Point out each malaria parasite.
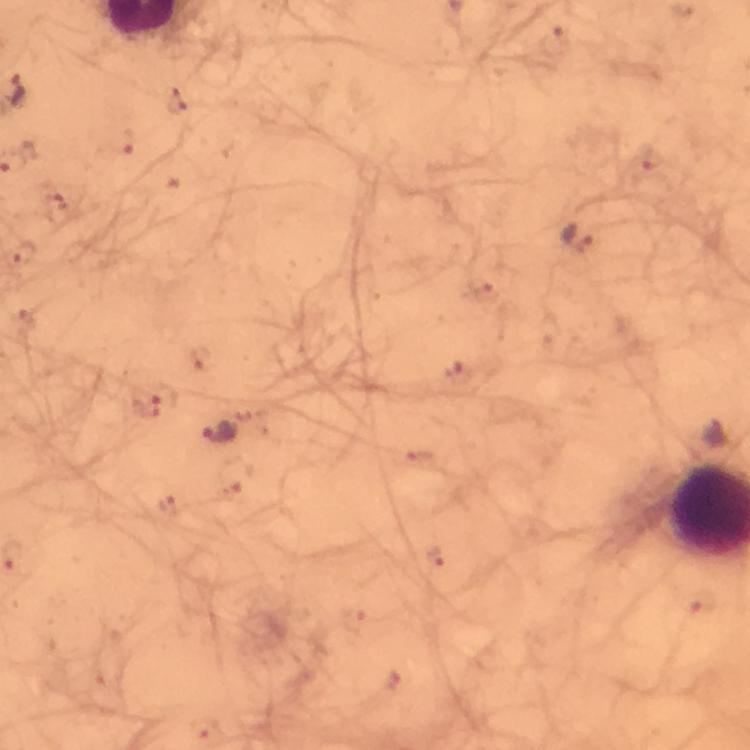

Approximate centers as {x, y} in pixels.
Malaria parasites: {555, 42}, {177, 103}, {126, 144}, {647, 159}, {54, 204}, {578, 238}, {24, 252}, {480, 286}, {201, 358}, {458, 373}, {147, 406}, {219, 432}, {423, 461}, {170, 505}, {435, 558}, {353, 622}, {204, 728}.

Giemsa-stained preparation. Photographed with a smartphone mounted on the microscope. Immersion oil applied. From a malaria diagnostic workup. Thick smear. Image is 750×750 pixels. Cropped region of a single field of view. 100x magnification.